Give the extent of all Plasmodium falciparum-infected red blood cells.
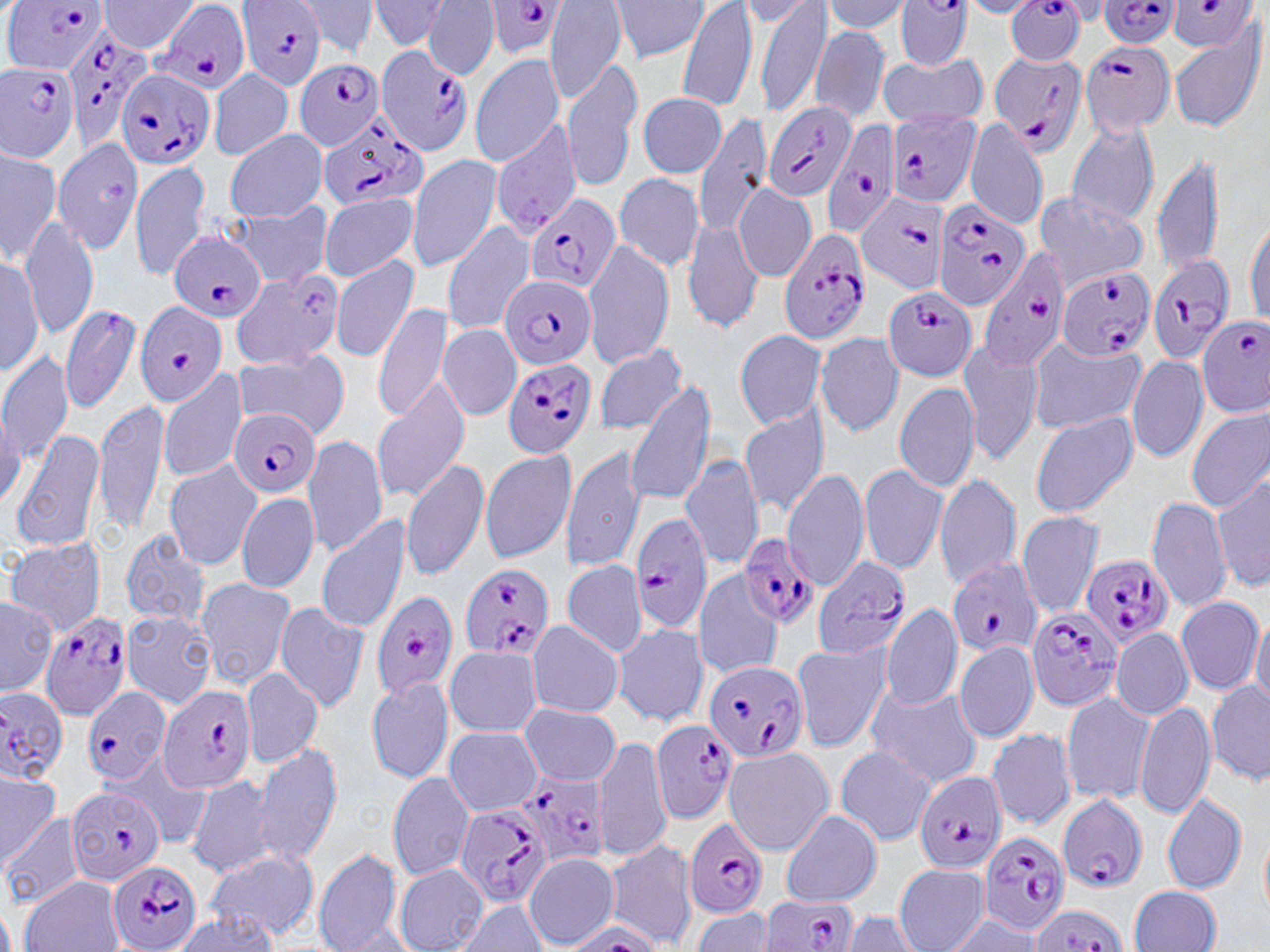
Approximate bounding boxes as (x1, y1, x2, y2) in pixels.
Plasmodium falciparum-infected red blood cells (subset): (3, 0, 108, 75), (238, 0, 326, 90), (895, 0, 971, 71), (1095, 0, 1182, 48), (155, 1, 251, 95), (480, 1, 572, 59), (1002, 2, 1091, 64), (59, 27, 154, 148), (1079, 38, 1175, 137), (376, 46, 471, 157), (989, 50, 1087, 155), (293, 59, 387, 149), (0, 61, 80, 162), (116, 67, 216, 172), (764, 101, 856, 202), (886, 109, 980, 207), (316, 113, 429, 213), (821, 120, 904, 239), (856, 192, 950, 295), (525, 193, 622, 297), (932, 199, 1029, 310), (777, 230, 874, 343), (170, 231, 265, 324), (976, 249, 1071, 368), (1144, 251, 1236, 364), (1055, 267, 1155, 362), (501, 276, 595, 369), (884, 285, 977, 380), (135, 302, 228, 407), (1198, 315, 1270, 415), (502, 356, 596, 459), (231, 407, 321, 499), (629, 512, 712, 636), (738, 534, 816, 629), (812, 556, 911, 659), (1082, 556, 1174, 646), (948, 560, 1041, 659), (459, 563, 556, 661), (369, 589, 458, 702), (1026, 607, 1122, 712), (38, 610, 133, 722), (702, 658, 810, 763), (158, 685, 258, 793), (80, 687, 172, 785), (0, 688, 70, 782), (651, 720, 738, 822), (516, 771, 611, 866), (913, 771, 1007, 874), (66, 786, 167, 885), (1055, 793, 1148, 893), (454, 805, 552, 908), (684, 818, 768, 918), (980, 831, 1070, 935), (108, 861, 204, 952), (757, 893, 863, 951), (1029, 905, 1125, 952).

Uninfected red blood cell locations (subset): (98, 0, 199, 54), (292, 0, 379, 58), (367, 0, 452, 52), (423, 0, 499, 78), (545, 0, 626, 102), (610, 0, 708, 64), (678, 0, 756, 113), (755, 0, 831, 116), (820, 1, 914, 35), (960, 1, 1044, 18), (1166, 21, 1266, 135), (808, 24, 890, 124), (877, 54, 986, 128), (468, 55, 564, 169), (561, 58, 643, 190), (209, 68, 292, 160), (637, 92, 727, 177), (693, 114, 772, 240), (964, 117, 1048, 229), (489, 119, 580, 238), (1066, 121, 1160, 225), (226, 129, 328, 224), (53, 137, 144, 258), (0, 146, 60, 267), (1151, 152, 1223, 275), (408, 155, 503, 272), (131, 160, 212, 282), (614, 173, 705, 271), (734, 183, 816, 282), (1031, 189, 1148, 292), (318, 193, 418, 283), (229, 199, 332, 289), (1245, 211, 1270, 327), (19, 214, 98, 340), (682, 218, 763, 332), (441, 222, 537, 334), (581, 238, 674, 369), (0, 253, 42, 379), (329, 256, 418, 361), (228, 274, 338, 372), (373, 301, 454, 421), (57, 302, 141, 414), (439, 323, 521, 420), (735, 330, 827, 428), (814, 333, 905, 438), (1027, 338, 1145, 433), (958, 339, 1044, 465), (592, 343, 689, 436), (0, 350, 72, 465), (232, 352, 349, 437), (1126, 354, 1208, 462), (158, 368, 249, 483), (371, 376, 471, 504), (895, 381, 980, 494), (626, 383, 719, 509), (93, 398, 169, 539), (0, 405, 25, 513), (738, 406, 830, 516), (1185, 406, 1270, 513), (1028, 411, 1138, 518), (10, 427, 106, 554), (301, 433, 388, 558), (560, 447, 649, 572), (479, 449, 576, 563), (679, 453, 765, 573), (402, 457, 490, 580), (164, 461, 260, 571), (858, 464, 948, 575), (780, 466, 870, 591), (933, 473, 1022, 589), (1212, 475, 1270, 591), (236, 492, 319, 594), (1147, 495, 1233, 613), (1016, 511, 1106, 618), (316, 516, 411, 636), (118, 530, 214, 631), (5, 538, 106, 635), (560, 562, 647, 656), (692, 569, 786, 680), (194, 577, 295, 690), (0, 595, 55, 697), (1176, 595, 1264, 694), (272, 601, 370, 714), (881, 602, 963, 711), (122, 609, 216, 709), (1250, 614, 1270, 710), (526, 620, 625, 716), (611, 622, 708, 727), (1113, 628, 1193, 719), (791, 640, 893, 752), (953, 641, 1039, 742), (444, 646, 542, 737), (241, 667, 323, 769), (365, 676, 453, 786), (1206, 678, 1270, 787), (863, 684, 985, 789), (1060, 693, 1152, 804), (1134, 700, 1215, 820), (520, 703, 619, 786), (443, 726, 542, 815), (985, 726, 1076, 830), (593, 732, 670, 862), (252, 742, 344, 867), (833, 746, 935, 845), (722, 747, 832, 855), (108, 753, 216, 849), (0, 768, 61, 865), (388, 772, 474, 880), (185, 774, 278, 878), (1161, 791, 1245, 894), (780, 810, 882, 906), (1, 812, 85, 907), (1258, 824, 1270, 923), (605, 838, 696, 948), (311, 848, 403, 950), (205, 850, 320, 941), (523, 854, 619, 948), (395, 864, 486, 951), (894, 865, 989, 952), (19, 875, 124, 952), (1129, 886, 1221, 951), (453, 899, 549, 951), (688, 908, 775, 951), (168, 912, 279, 951), (841, 912, 923, 951), (944, 914, 1046, 950). Platelet locations: (104, 178, 129, 204). Slide-level diagnosis: Plasmodium falciparum. May-Grünwald-Giemsa-stained preparation. Image is 1270×952 pixels. Thin blood smear. Optical microscopy. One field of a larger specimen. Captured at 1000x magnification.